Locate every blood parasite and identify its species.
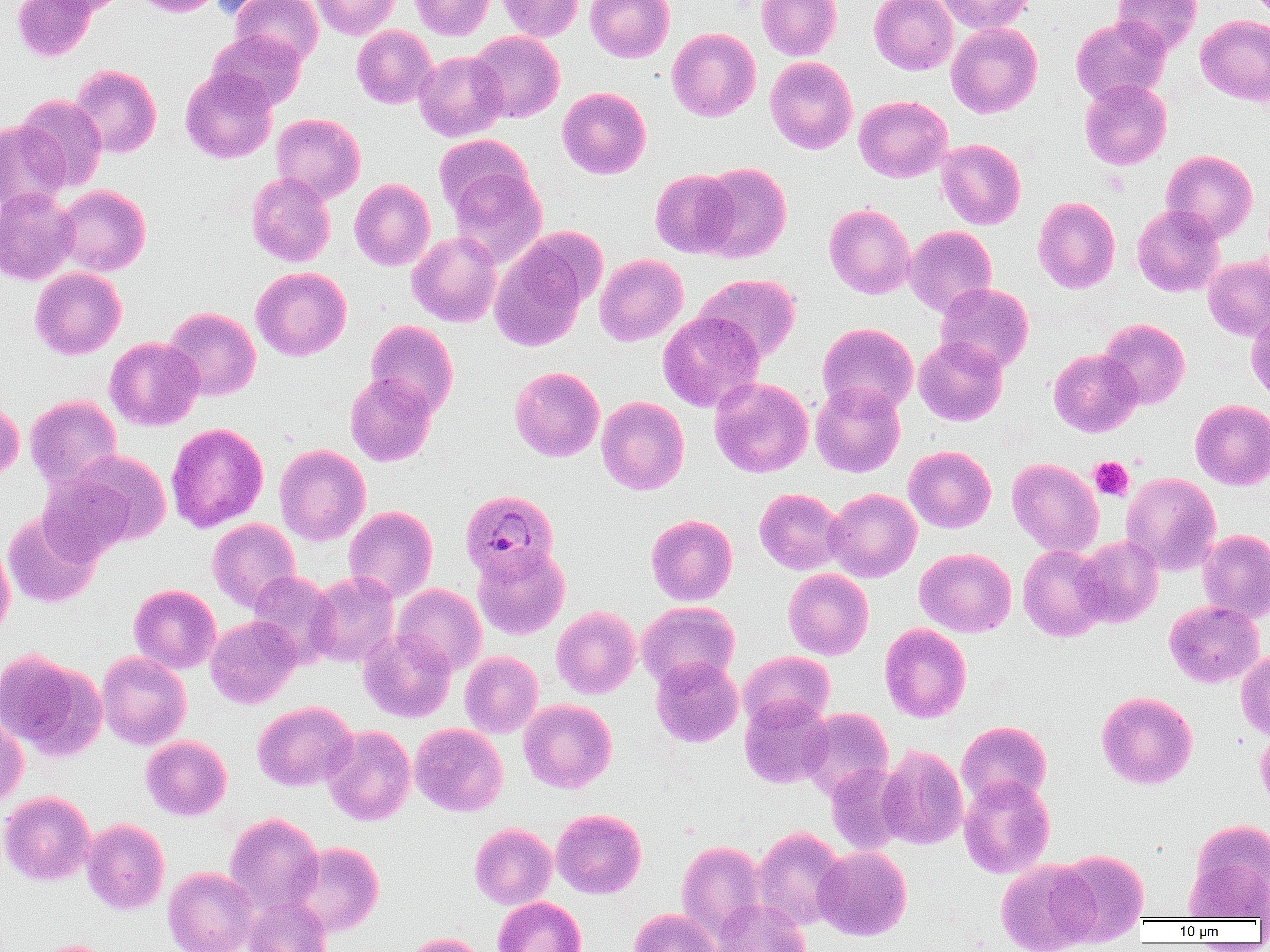

Approximate bounding boxes as (x1, y1, x2, y2) in pixels.
Plasmodium ovale-infected red blood cells: (461, 489, 558, 581).
No Plasmodium falciparum, Plasmodium malariae, Plasmodium vivax, Babesia divergens, or Trypanosoma brucei observed.

Platelet locations: (1089, 457, 1133, 500). Uninfected red blood cell locations: (13, 0, 97, 62), (41, 0, 129, 16), (133, 0, 223, 17), (209, 0, 289, 20), (231, 0, 322, 67), (311, 0, 399, 39), (409, 0, 495, 40), (497, 0, 583, 41), (585, 0, 674, 62), (756, 0, 841, 60), (869, 0, 958, 75), (934, 0, 1035, 34), (1112, 0, 1202, 57), (1196, 14, 1270, 105), (1070, 16, 1170, 105), (946, 22, 1042, 118), (352, 25, 437, 108), (667, 27, 760, 121), (207, 30, 306, 111), (469, 31, 564, 122), (413, 50, 508, 142), (765, 57, 857, 154), (70, 65, 162, 157), (180, 68, 278, 163), (1080, 79, 1171, 169), (557, 87, 651, 179), (16, 94, 108, 192), (854, 95, 951, 182), (272, 113, 365, 203), (0, 120, 69, 213), (433, 134, 533, 217), (936, 139, 1026, 229), (1161, 149, 1258, 242), (697, 162, 792, 263), (650, 168, 740, 258), (448, 169, 546, 267), (246, 172, 336, 266), (350, 179, 435, 270), (55, 184, 151, 275), (0, 187, 79, 285), (1032, 197, 1120, 294), (824, 204, 915, 299), (1131, 204, 1225, 296), (905, 225, 997, 317), (407, 231, 502, 327), (489, 241, 590, 351), (594, 254, 688, 346), (1203, 255, 1270, 341), (29, 267, 126, 359), (251, 267, 351, 360), (695, 273, 801, 363), (935, 282, 1034, 373), (163, 307, 261, 400), (658, 311, 764, 413), (1246, 311, 1270, 404), (1098, 318, 1190, 409), (365, 320, 458, 417), (817, 323, 918, 416), (914, 336, 1008, 426), (105, 337, 204, 431), (1048, 348, 1141, 437), (509, 366, 604, 461), (344, 373, 437, 466), (710, 377, 814, 478), (810, 381, 905, 477), (25, 394, 122, 489), (597, 396, 689, 494), (0, 399, 24, 482), (1190, 399, 1270, 490), (165, 423, 268, 532), (274, 444, 370, 545), (904, 445, 996, 533), (56, 450, 172, 550), (1007, 457, 1104, 557), (1121, 472, 1221, 575), (754, 488, 846, 575), (824, 488, 922, 582), (343, 505, 437, 603), (2, 511, 101, 609), (646, 514, 737, 606), (208, 518, 300, 611), (1198, 529, 1270, 622), (1074, 536, 1163, 627), (0, 541, 15, 639), (1018, 544, 1110, 641), (473, 545, 569, 639), (914, 547, 1015, 636), (783, 568, 873, 660), (247, 571, 340, 667), (306, 571, 399, 667), (129, 584, 221, 674), (393, 584, 486, 676), (1163, 600, 1264, 688), (637, 601, 739, 689), (551, 606, 640, 699), (205, 615, 301, 708), (879, 623, 972, 722), (357, 628, 456, 723), (1236, 647, 1270, 740), (0, 650, 107, 761), (96, 651, 191, 749), (460, 651, 543, 738), (739, 651, 835, 730), (651, 655, 743, 747), (1096, 691, 1198, 789), (739, 695, 833, 789), (519, 699, 616, 793), (252, 700, 357, 791), (799, 707, 893, 801), (0, 712, 28, 806), (956, 721, 1052, 807), (410, 723, 507, 816), (323, 726, 416, 825), (1256, 728, 1270, 812), (141, 735, 232, 820), (877, 744, 968, 849), (826, 763, 910, 855), (959, 775, 1055, 878), (0, 791, 95, 885), (551, 808, 646, 898), (224, 813, 324, 915), (81, 818, 169, 914), (1187, 818, 1270, 917), (469, 822, 557, 909), (752, 826, 847, 930), (676, 840, 767, 938), (289, 841, 384, 936), (814, 846, 912, 940), (1050, 848, 1149, 945), (995, 859, 1101, 951), (162, 866, 258, 952), (244, 897, 332, 952), (494, 897, 585, 952), (711, 899, 811, 952), (629, 908, 720, 952), (403, 933, 486, 952), (26, 939, 118, 952). Slide-level diagnosis: Plasmodium ovale. Single field of view. Image is 1270×952 pixels. Light microscopy. Thin blood smear. 1000x magnification.